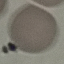

{
  "result": "no malaria parasites seen",
  "image_type": "cell patch, automatically extracted from a larger field of view and resized to 64 × 64 pixels",
  "preparation": "thin smear",
  "capture": "smartphone camera at the microscope eyepiece",
  "stain": "Giemsa"
}